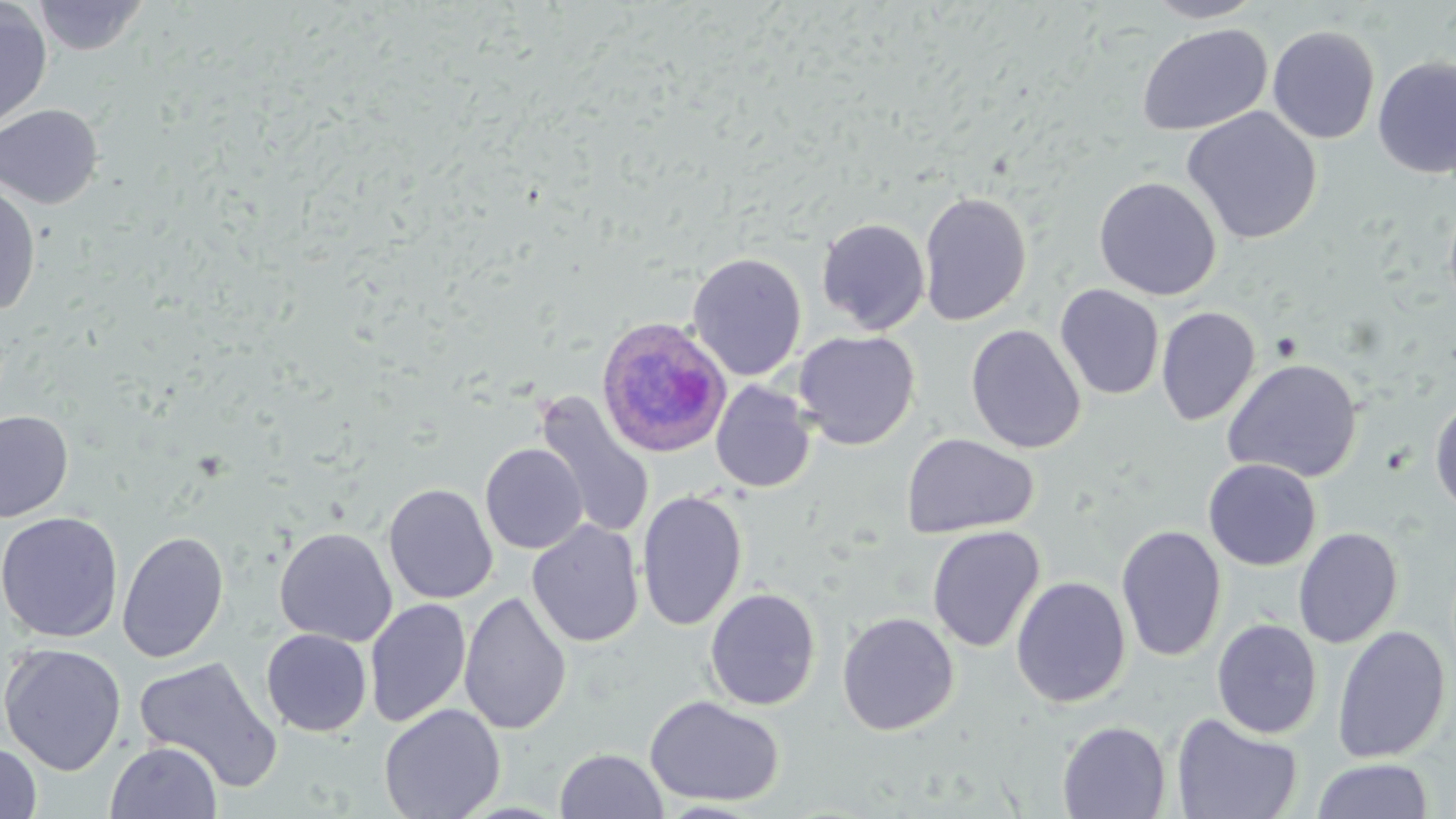

Approximate bounding boxes as [x1, y1, x2, y2] in pixels. Plasmodium ovale-infected red blood cell locations: [595, 316, 732, 457]. Uninfected red blood cell locations: [32, 0, 148, 57], [1143, 0, 1266, 23], [0, 2, 53, 133], [1136, 23, 1273, 137], [1266, 24, 1381, 144], [1372, 55, 1456, 179], [0, 104, 103, 208], [1182, 106, 1322, 244], [1094, 176, 1222, 300], [0, 183, 41, 317], [919, 191, 1032, 326], [1443, 197, 1456, 321], [816, 217, 931, 335], [687, 252, 807, 381], [1055, 284, 1164, 400], [1156, 306, 1260, 426], [965, 324, 1086, 454], [792, 330, 920, 450], [1222, 358, 1363, 483], [710, 380, 816, 493], [533, 390, 655, 540], [1429, 397, 1456, 516], [0, 410, 74, 522], [901, 432, 1038, 539], [480, 443, 587, 554], [1203, 458, 1321, 571], [383, 483, 498, 604], [636, 489, 748, 631], [0, 511, 123, 642], [527, 520, 645, 648], [1115, 524, 1227, 662], [926, 525, 1045, 652], [274, 526, 397, 647], [1293, 527, 1403, 648], [117, 530, 229, 663], [1011, 576, 1131, 708], [704, 587, 822, 710], [458, 590, 572, 736], [364, 598, 471, 727], [837, 611, 959, 735], [1211, 618, 1323, 739], [1331, 625, 1451, 764], [261, 629, 372, 737], [1, 642, 127, 776], [133, 655, 284, 793], [644, 694, 785, 807], [379, 704, 505, 819], [1170, 712, 1303, 819], [1057, 720, 1172, 818], [105, 740, 223, 818], [0, 741, 42, 818], [555, 748, 668, 819], [1311, 758, 1434, 819]. Slide-level diagnosis: Plasmodium ovale. May-Grünwald-Giemsa-stained preparation. 1000x magnification. Image is 1456×819 pixels. Thin blood film. Optical microscopy. One field of a larger specimen.